Report the malaria status of this cell.
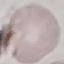

It is uninfected.

Summary:
  - Image type: cell patch, automatically extracted from a larger field of view and resized to 64 × 64 pixels
  - Preparation: thin smear
  - Stain: Giemsa
  - Capture: smartphone through the microscope eyepiece